Locate every WBC.
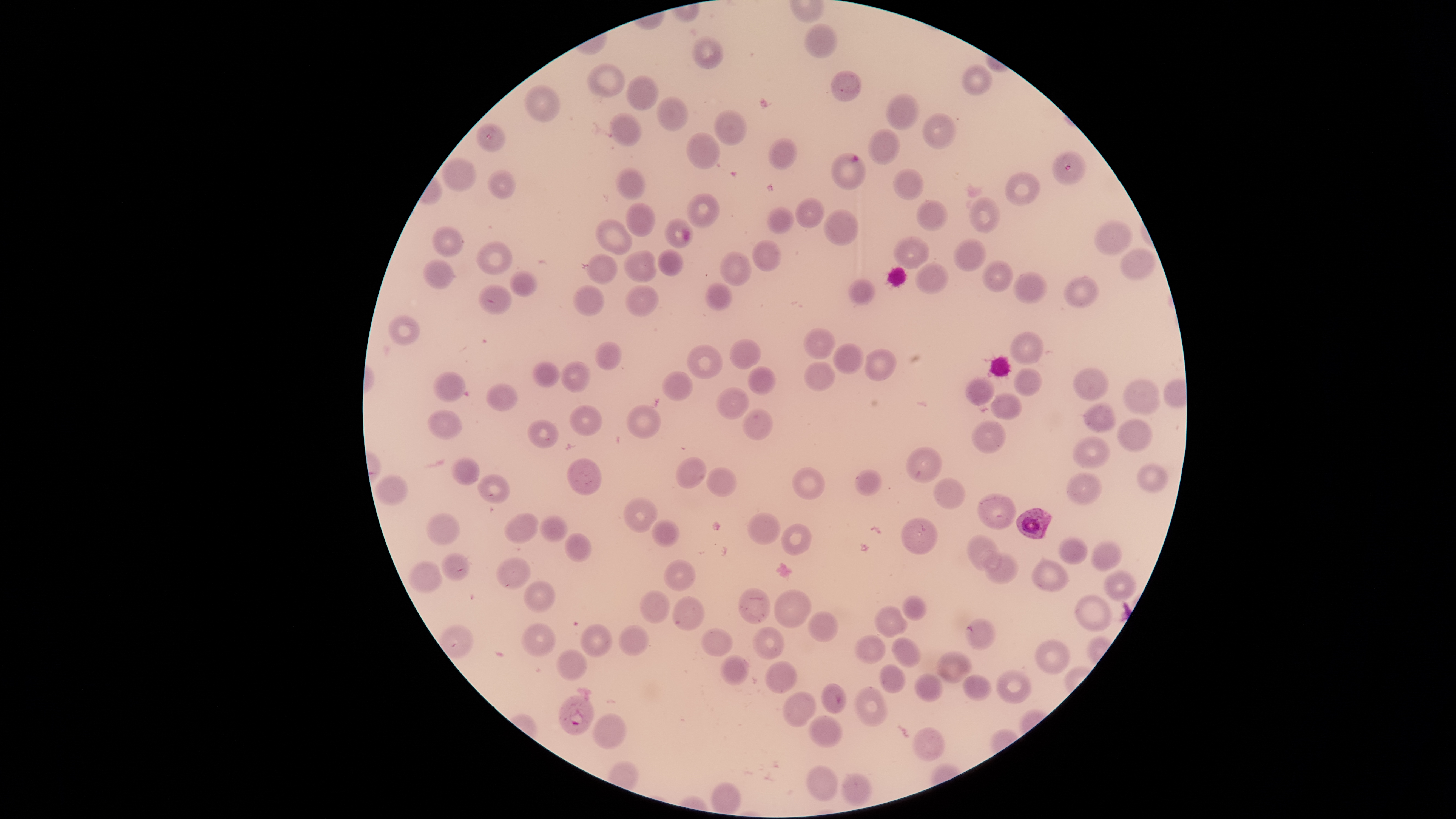
No WBCs identified.

Approximate bounding boxes as [left, top, right, bottom] in pixels.
Summary:
  - Parasitized RBCs: [1052, 152, 1086, 186], [829, 153, 866, 189], [1016, 507, 1053, 540], [556, 695, 595, 735]
  - Uninfected RBCs: [803, 23, 838, 59], [693, 36, 724, 69], [586, 63, 625, 97], [962, 64, 993, 97], [831, 69, 862, 102], [627, 76, 659, 111], [525, 86, 561, 122], [886, 95, 919, 131], [656, 97, 687, 131], [714, 109, 746, 146], [609, 112, 643, 147], [921, 112, 956, 149], [476, 123, 506, 152], [866, 128, 900, 165], [686, 133, 719, 168], [768, 138, 798, 171], [442, 159, 476, 192], [892, 167, 923, 200], [487, 169, 514, 200], [616, 169, 645, 199], [1004, 172, 1039, 206], [688, 194, 719, 228], [795, 198, 823, 229], [967, 198, 1000, 234], [917, 201, 948, 231], [626, 204, 654, 237], [767, 207, 794, 234], [823, 209, 859, 247], [665, 217, 693, 248], [595, 218, 632, 255], [1094, 220, 1133, 256], [430, 226, 463, 258], [894, 236, 929, 269], [953, 238, 986, 271], [750, 240, 781, 272], [475, 242, 511, 275], [1120, 248, 1157, 280], [657, 250, 682, 276], [719, 250, 750, 287], [623, 251, 658, 282], [586, 254, 617, 284], [423, 259, 454, 289], [982, 260, 1015, 292], [916, 264, 948, 295], [509, 272, 537, 297], [1014, 272, 1048, 305], [1063, 276, 1099, 308], [848, 278, 874, 305], [704, 283, 733, 311], [475, 285, 512, 315], [573, 285, 605, 317], [625, 285, 659, 318], [388, 316, 419, 345], [804, 327, 833, 360], [1010, 332, 1044, 363], [729, 339, 760, 369], [595, 341, 621, 372], [833, 343, 865, 374], [687, 345, 723, 380], [863, 348, 896, 381], [533, 360, 560, 387], [561, 361, 590, 391], [804, 362, 836, 392], [747, 366, 775, 395], [1014, 367, 1042, 396], [1072, 368, 1108, 399], [662, 371, 693, 402], [432, 372, 465, 403], [965, 379, 995, 405], [1122, 379, 1160, 416], [485, 383, 518, 411], [715, 388, 749, 419], [991, 392, 1021, 420], [1085, 401, 1116, 432], [569, 405, 603, 436], [626, 405, 660, 439], [742, 409, 773, 441], [428, 410, 462, 440], [526, 419, 559, 448], [1117, 419, 1151, 451], [972, 420, 1005, 454], [1073, 436, 1110, 470], [907, 446, 941, 482], [675, 456, 707, 488], [451, 457, 480, 484], [567, 458, 601, 496], [1138, 463, 1168, 494], [792, 467, 825, 499], [705, 469, 738, 496], [854, 469, 883, 496], [1065, 473, 1102, 506], [477, 474, 510, 504], [375, 475, 409, 505], [933, 477, 966, 509], [978, 493, 1017, 528], [623, 497, 658, 533], [503, 511, 538, 544], [748, 512, 780, 545], [426, 513, 461, 546], [542, 516, 567, 542], [899, 516, 938, 554], [652, 519, 679, 546], [781, 521, 814, 555], [564, 533, 591, 561], [966, 536, 1002, 571], [1058, 536, 1088, 564], [1090, 540, 1121, 571], [983, 551, 1017, 583], [440, 553, 469, 581], [496, 555, 529, 588], [663, 559, 696, 591], [1030, 560, 1069, 592], [409, 561, 443, 592], [1104, 569, 1137, 599], [523, 581, 555, 612], [738, 588, 771, 622], [774, 588, 812, 628], [639, 589, 670, 622], [1075, 593, 1112, 630], [673, 595, 705, 630], [903, 595, 926, 620], [873, 606, 910, 637], [808, 611, 839, 642], [965, 619, 995, 648], [521, 623, 556, 657], [579, 624, 613, 657], [618, 624, 650, 656], [752, 626, 783, 659], [701, 627, 732, 656], [855, 635, 886, 663], [892, 638, 922, 667], [1035, 638, 1071, 674], [556, 648, 587, 679], [936, 650, 972, 683], [720, 654, 750, 686], [765, 660, 797, 693], [880, 664, 907, 693], [995, 669, 1032, 702], [914, 673, 943, 701], [962, 674, 992, 700], [821, 683, 847, 714], [855, 687, 888, 726], [783, 691, 815, 727], [592, 713, 626, 750], [808, 716, 843, 747], [912, 728, 945, 761], [807, 764, 838, 801], [842, 771, 873, 805]
  - Capture: smartphone photograph through the microscope eyepiece
  - Image size: 1456×819 pixels
  - Species: Plasmodium falciparum
  - Presence: malaria parasites identified
  - Preparation: thin blood smear
  - Stain: Giemsa
  - Field of view: single
  - Visible region: circular